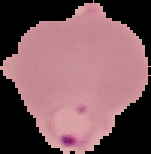

preparation = thin blood film
image type = segmented cell region with the area outside set to black
result = malaria parasites detected
image size = 151×154 pixels